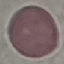
Summary:
  - Result: no malaria parasites seen
  - Preparation: thin blood film
  - Capture: smartphone through the microscope eyepiece
  - Stain: Giemsa
  - Image type: cell patch, automatically extracted from a larger field of view and resized to 64 × 64 pixels